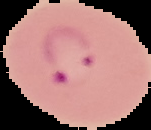 From a thin blood smear. Image is 151×130 pixels. The area outside the segmented cell region is set to black. Result: Plasmodium parasites detected.